Point out every malaria parasite and every leukocyte.
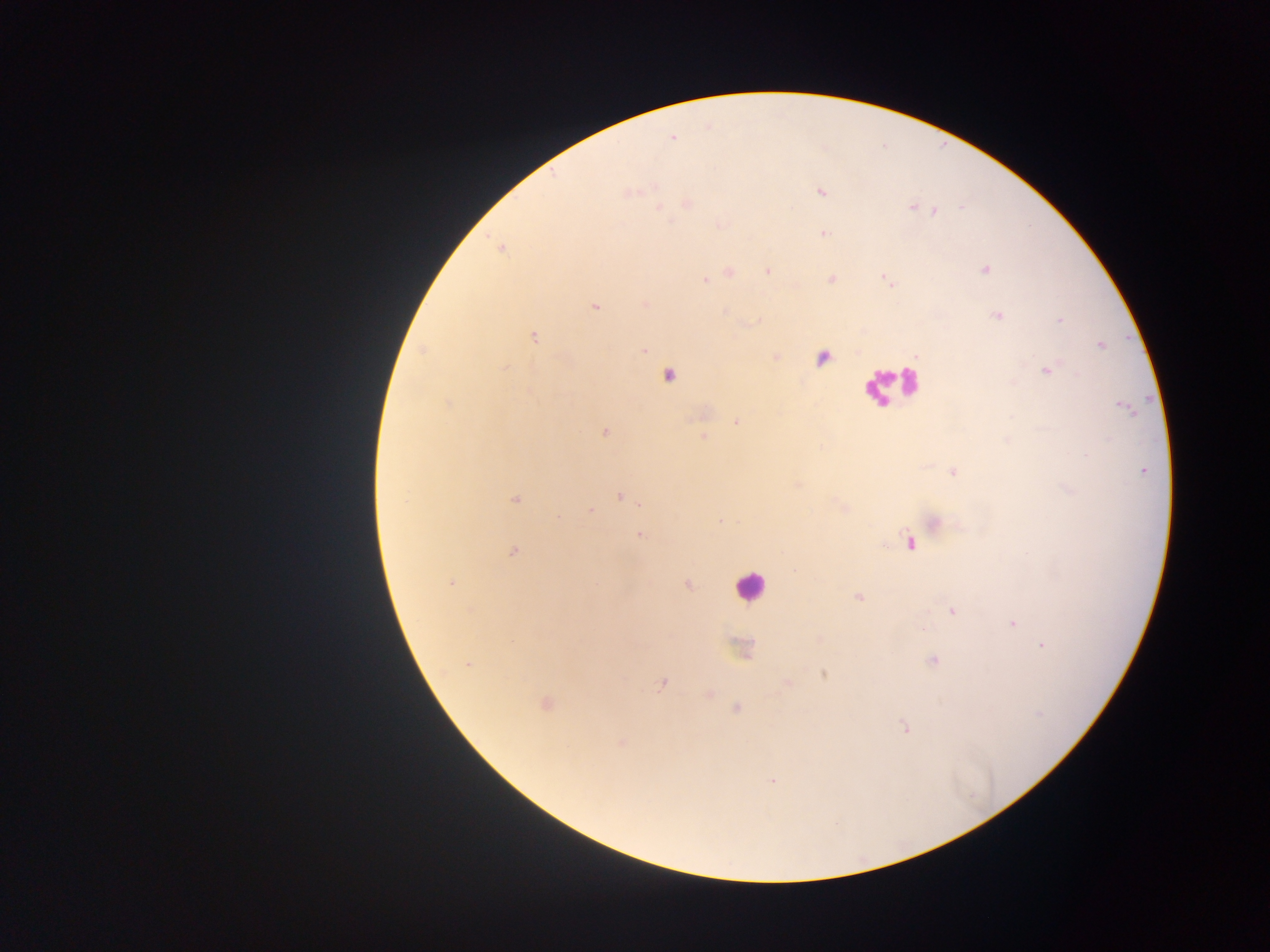

Approximate centers as {x, y} in pixels.
Malaria parasites: {821, 192}, {911, 208}, {961, 208}, {933, 211}, {823, 233}, {767, 270}, {831, 277}, {705, 280}, {645, 305}, {595, 307}, {1058, 321}, {534, 337}, {1100, 345}, {644, 350}, {775, 356}, {504, 368}, {1045, 371}, {736, 421}, {604, 432}, {702, 434}, {951, 471}, {620, 496}, {514, 499}, {638, 502}, {589, 511}, {557, 517}, {720, 520}, {903, 532}, {640, 534}, {514, 550}, {451, 582}, {688, 584}, {858, 596}, {951, 610}, {1012, 623}, {1042, 645}, {469, 663}, {662, 683}, {903, 726}, {622, 741}, {773, 781}.
Leukocytes: {752, 585}.

country = Ghana
image size = 1270×952 pixels
field of view = single
capture = mobile-phone photograph through a microscope
preparation = thick blood film